Comment on the morphology of the erythrocytes.
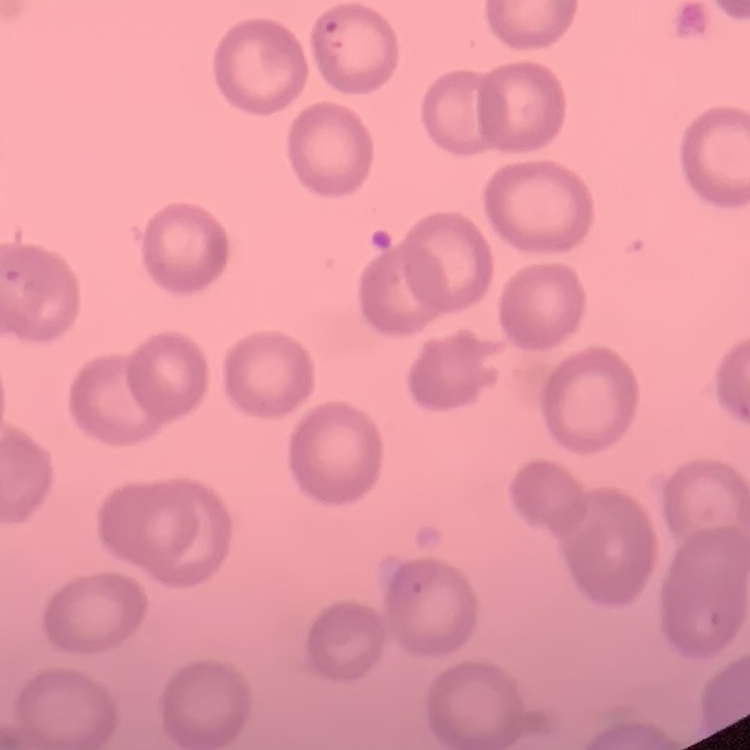
They show no rouleaux formation.

Summary:
  - Preparation: thin peripheral smear
  - Image type: one tile cut from a larger photomicrograph
  - Stain: Field's or Giemsa